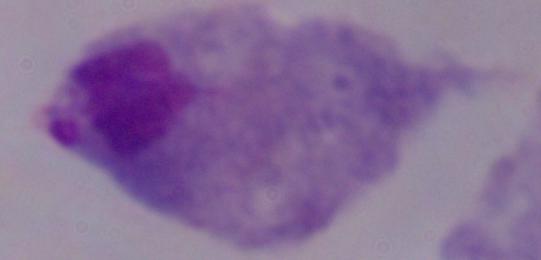
identification: trichomonad
modality: photomicrograph
magnification: 1000x